Describe the morphology of the red blood cells.
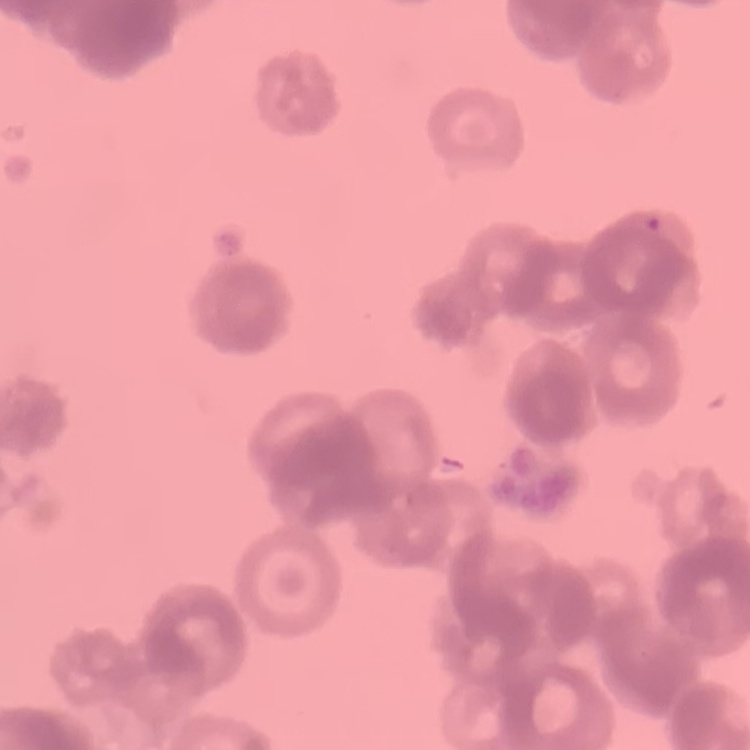

They show rouleaux formation.

One tile cut from a larger photomicrograph. Stained with either Field's or Giemsa. Thin peripheral smear.